Name the blood parasite species.
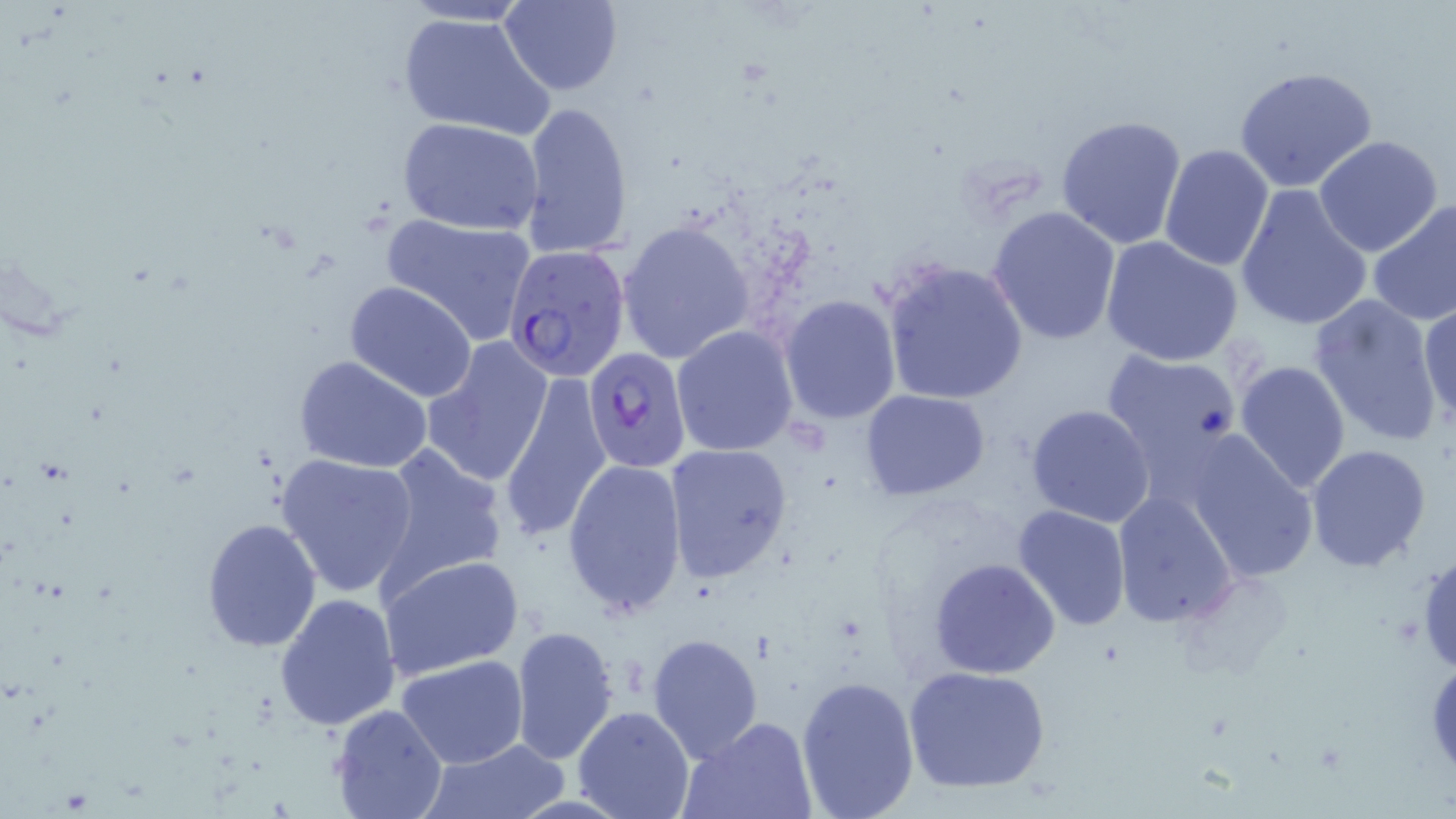
Plasmodium falciparum.

Approximate bounding boxes as named x1/y1/x2/y2 corners in pixels. Plasmodium falciparum-infected red blood cell locations: (x1=503, y1=245, x2=630, y2=380), (x1=585, y1=344, x2=693, y2=474). Uninfected red blood cell locations: (x1=498, y1=1, x2=624, y2=94), (x1=397, y1=10, x2=554, y2=139), (x1=1234, y1=65, x2=1380, y2=195), (x1=518, y1=100, x2=635, y2=259), (x1=1056, y1=115, x2=1189, y2=252), (x1=397, y1=116, x2=545, y2=237), (x1=1313, y1=135, x2=1443, y2=258), (x1=1159, y1=143, x2=1275, y2=272), (x1=1234, y1=184, x2=1373, y2=331), (x1=1366, y1=198, x2=1456, y2=327), (x1=987, y1=205, x2=1122, y2=345), (x1=380, y1=214, x2=538, y2=342), (x1=618, y1=220, x2=754, y2=363), (x1=1100, y1=236, x2=1245, y2=368), (x1=882, y1=259, x2=1029, y2=404), (x1=343, y1=280, x2=479, y2=402), (x1=1308, y1=291, x2=1445, y2=448), (x1=779, y1=294, x2=902, y2=423), (x1=1418, y1=296, x2=1455, y2=432), (x1=671, y1=325, x2=799, y2=456), (x1=422, y1=337, x2=554, y2=487), (x1=1099, y1=348, x2=1245, y2=482), (x1=294, y1=355, x2=436, y2=474), (x1=1233, y1=360, x2=1352, y2=493), (x1=501, y1=372, x2=609, y2=545), (x1=859, y1=390, x2=991, y2=499), (x1=1025, y1=405, x2=1156, y2=528), (x1=1182, y1=431, x2=1319, y2=584), (x1=663, y1=444, x2=796, y2=585), (x1=1306, y1=444, x2=1433, y2=573), (x1=376, y1=445, x2=509, y2=590), (x1=275, y1=452, x2=420, y2=596), (x1=562, y1=457, x2=690, y2=618), (x1=1112, y1=492, x2=1240, y2=627), (x1=1011, y1=504, x2=1130, y2=631), (x1=201, y1=519, x2=322, y2=651), (x1=379, y1=554, x2=524, y2=681), (x1=929, y1=559, x2=1060, y2=679), (x1=274, y1=591, x2=403, y2=730), (x1=510, y1=626, x2=619, y2=766), (x1=647, y1=633, x2=764, y2=760), (x1=397, y1=656, x2=528, y2=769), (x1=903, y1=665, x2=1053, y2=795), (x1=795, y1=675, x2=921, y2=818), (x1=332, y1=703, x2=448, y2=818), (x1=573, y1=705, x2=693, y2=819), (x1=680, y1=717, x2=817, y2=819), (x1=423, y1=740, x2=565, y2=818). May-Grünwald-Giemsa-stained preparation. Thin blood film. One field of a larger specimen. Image is 1456×819 pixels. Optical microscopy. 1000x magnification.